Identify the cell.
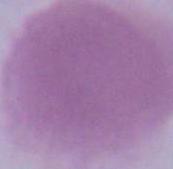

An erythrocyte.

Summary:
  - Magnification: 1000x
  - Modality: micrograph